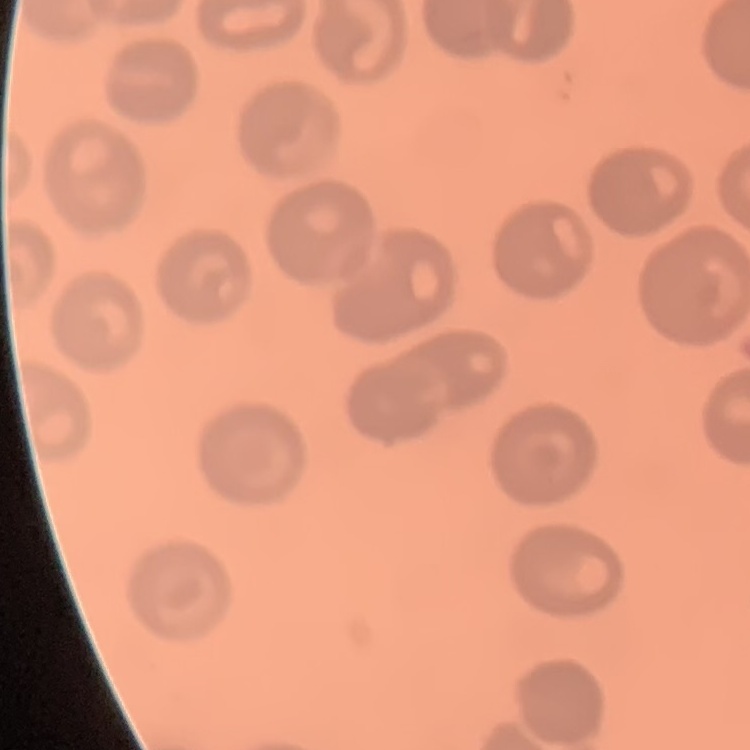
The red blood cells exhibit no rouleaux formation. Thin blood smear. One tile cut from a larger photomicrograph. Field's or Giemsa stain.